Describe the morphology of the red blood cells.
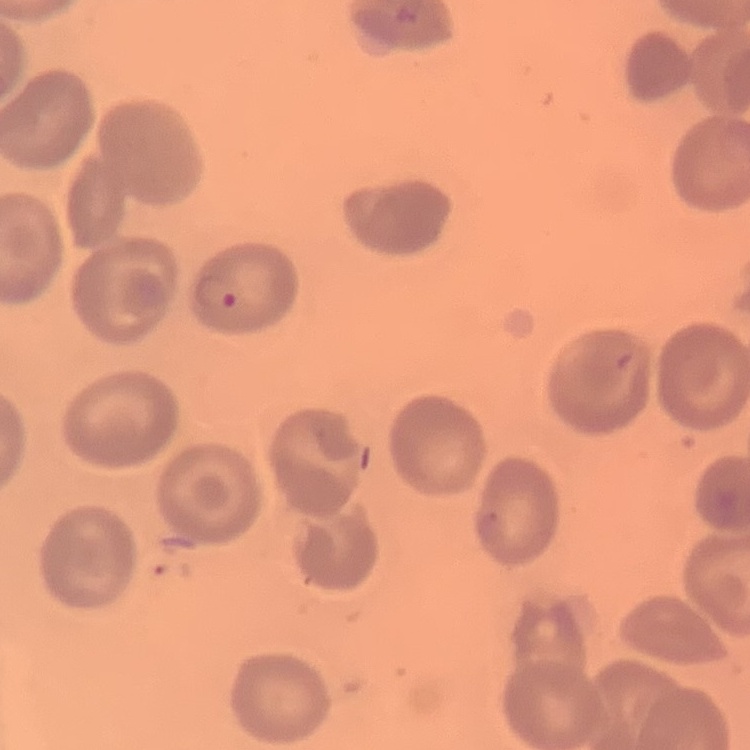

They show no rouleaux formation.

image type = one tile cut from a larger photomicrograph
preparation = thin blood smear
stain = Field's or Giemsa